Comment on the morphology of the red blood cells.
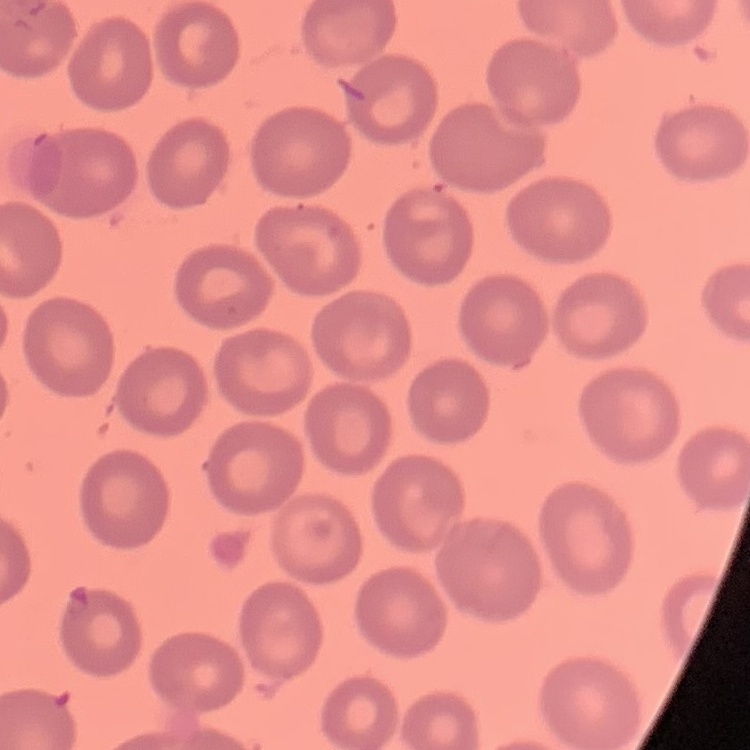

They show no rouleaux formation.

Thin blood smear. Stained with either Field's or Giemsa. Square crop of a larger photomicrograph.